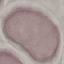

Summary:
  - Malaria status: uninfected
  - Stain: Giemsa
  - Preparation: thin blood smear
  - Image type: automatically extracted cell patch, resized to 64 × 64 pixels
  - Capture: smartphone camera at the microscope eyepiece